Comment on the morphology of the red blood cells.
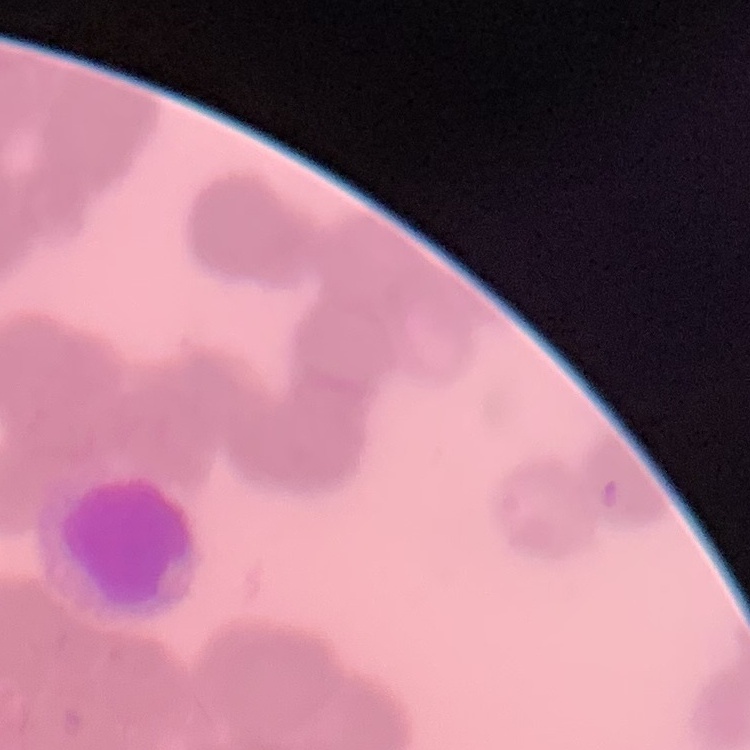

They show rouleaux formation.

stain = Field's or Giemsa
image type = one tile cut from a larger photomicrograph
preparation = thin peripheral smear